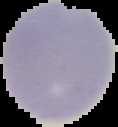

Image is 118×127 pixels. From a thin blood film. Cell region segmented out of the field of view; the surrounding area is masked to black. Malaria status: uninfected.